State the preparation type.
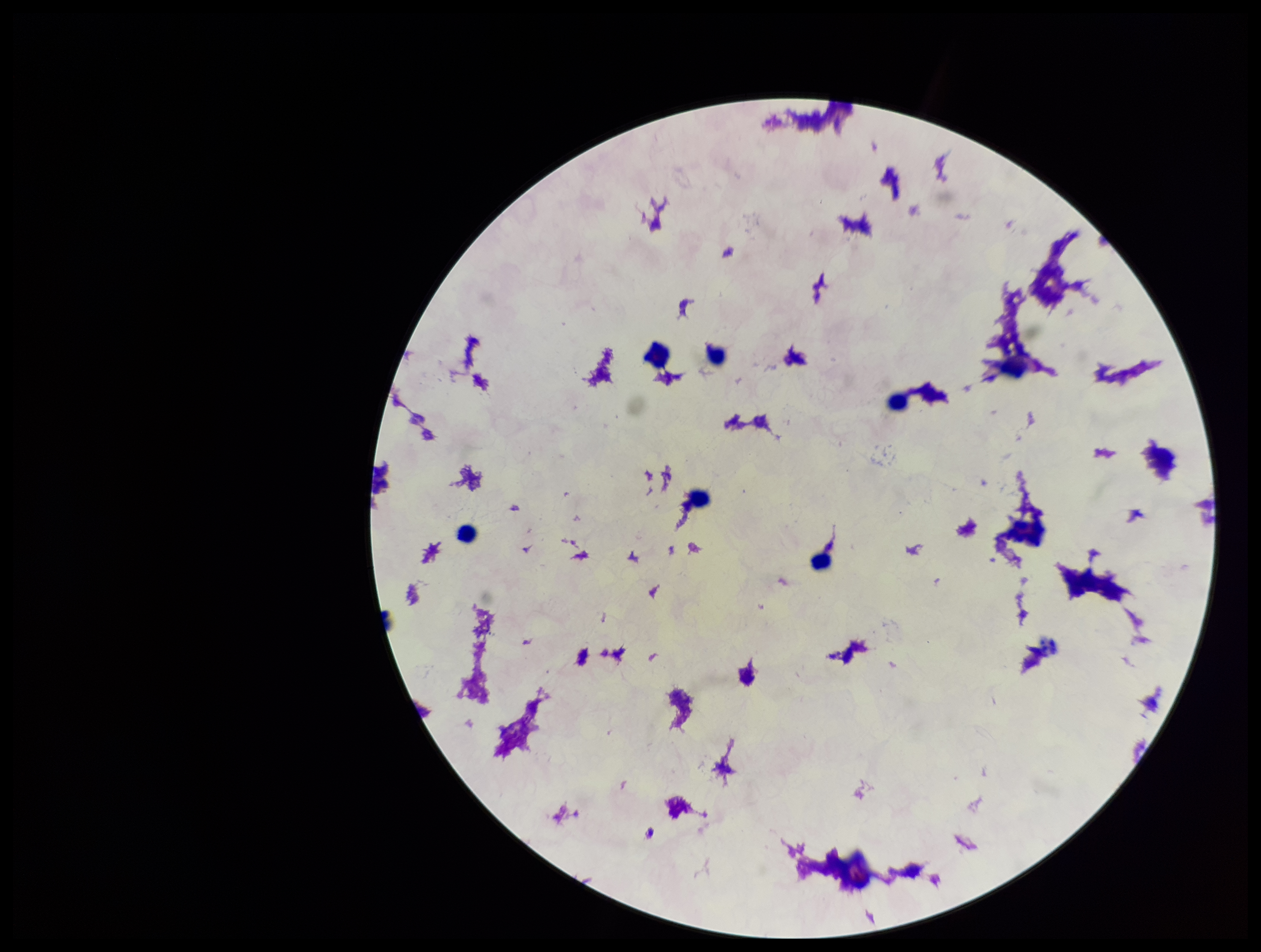
It is a thick blood smear.

{
  "image_size": "1261×952 pixels",
  "capture": "smartphone photograph through the microscope eyepiece",
  "field_of_view": "single",
  "plasmodium_parasites": "none identified",
  "parasite_count": 0,
  "patient_malaria_status": "negative",
  "leukocyte_count": 6,
  "stain": "Giemsa"
}